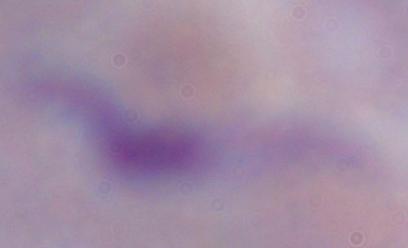
identification: trypanosome
modality: micrograph
magnification: 1000x